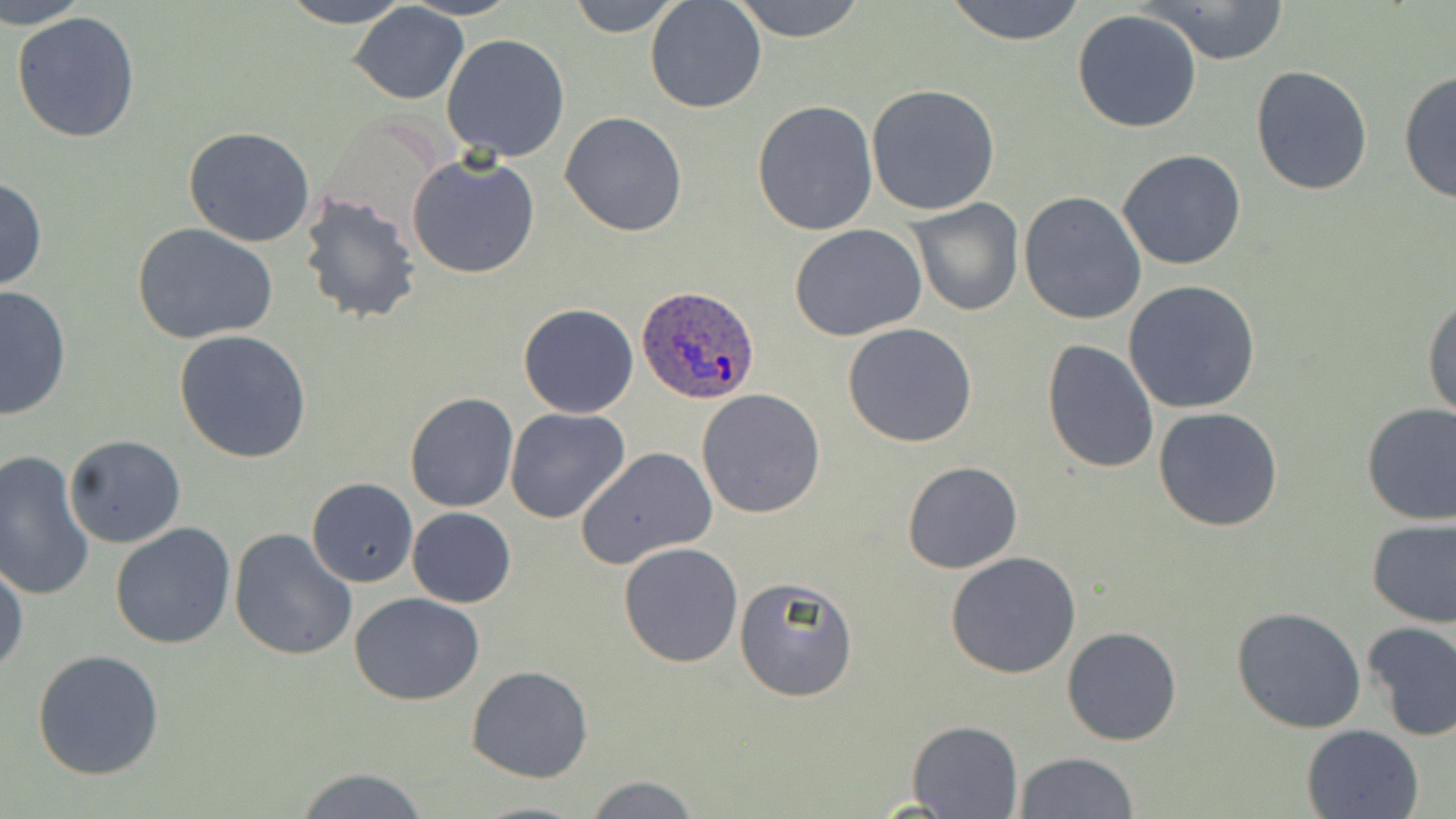

Approximate bounding boxes as (x1, y1, x2, y2) in pixels. Plasmodium ovale-infected red blood cell locations: (638, 285, 761, 404). Uninfected red blood cell locations: (2, 0, 92, 28), (279, 0, 413, 27), (401, 0, 521, 20), (567, 0, 683, 37), (645, 0, 767, 113), (728, 0, 869, 41), (943, 0, 1089, 44), (1142, 0, 1291, 65), (347, 2, 470, 105), (1072, 9, 1202, 133), (10, 10, 142, 145), (442, 32, 570, 160), (1250, 63, 1374, 196), (1398, 68, 1455, 206), (865, 83, 1001, 215), (752, 98, 878, 235), (559, 111, 687, 237), (184, 125, 315, 247), (1117, 148, 1247, 271), (407, 152, 541, 280), (0, 176, 48, 292), (296, 190, 422, 325), (1018, 191, 1147, 325), (907, 198, 1025, 317), (790, 223, 928, 341), (134, 224, 278, 347), (1122, 280, 1261, 415), (0, 285, 72, 420), (1423, 292, 1456, 422), (517, 302, 639, 418), (842, 323, 980, 448), (173, 331, 312, 462), (1042, 338, 1160, 472), (695, 388, 826, 519), (404, 392, 519, 512), (1359, 401, 1456, 526), (1154, 407, 1285, 532), (505, 409, 631, 526), (63, 435, 187, 549), (575, 446, 717, 568), (0, 447, 97, 601), (902, 462, 1022, 573), (76, 464, 215, 623), (306, 478, 417, 587), (406, 507, 516, 607), (1365, 516, 1455, 629), (110, 522, 236, 650), (227, 527, 358, 660), (618, 542, 744, 667), (947, 552, 1082, 678), (0, 555, 26, 677), (734, 578, 859, 701), (350, 594, 484, 707), (1231, 606, 1366, 733), (1361, 620, 1456, 742), (1062, 627, 1182, 746), (31, 648, 164, 779), (466, 665, 592, 783), (907, 720, 1023, 817), (1301, 724, 1424, 819), (1015, 751, 1139, 818), (293, 767, 430, 819), (581, 775, 702, 818), (467, 800, 594, 818). Slide-level diagnosis: Plasmodium ovale. Light microscopy. 1000x magnification. One field of a larger specimen. Thin blood film. May-Grünwald-Giemsa stain. Image is 1456×819 pixels.